Classify this cell by malaria status.
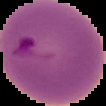
Parasitized.

From a thin blood film. Image is 106×106 pixels. Segmented cell region on a black background.